State which parasite is depicted.
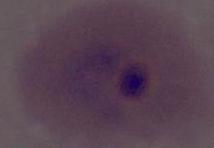

Plasmodium.

Micrograph. Captured at either 400x or 1000x magnification.